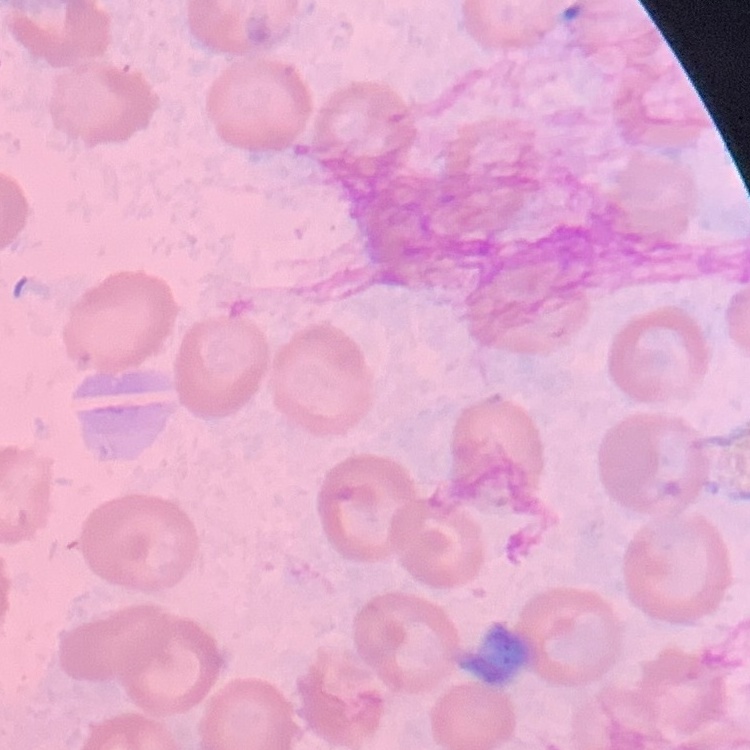 The erythrocytes exhibit no rouleaux formation. Thin peripheral smear. One tile cut from a larger photomicrograph. Stained with either Field's or Giemsa.